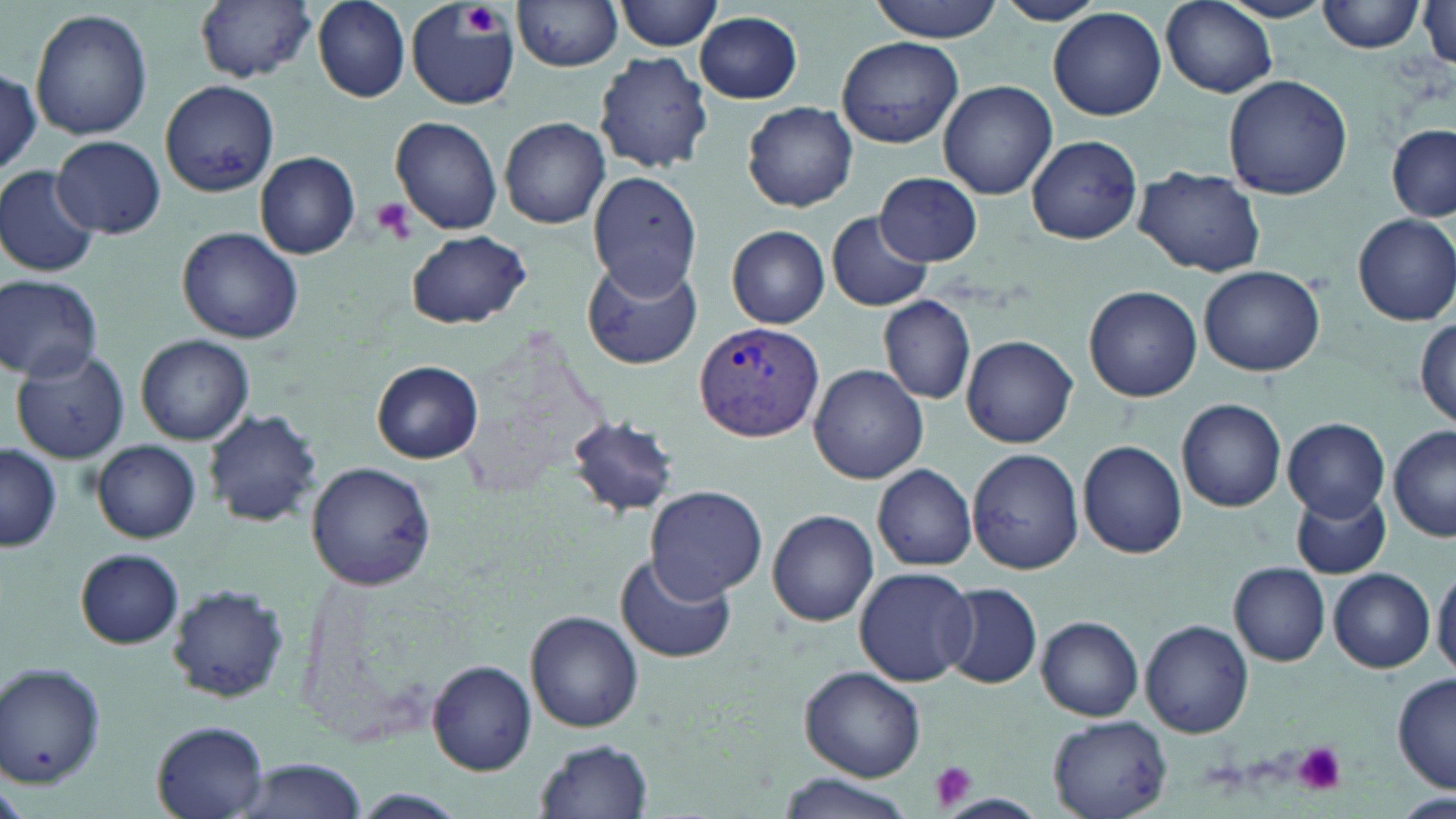
slide_level_diagnosis: Plasmodium vivax
platelet_locations: 'approximate bounding boxes as [x1, y1, x2, y2] in pixels: [460, 6, 506, 34], [370, 197, 416, 245], [1294, 742, 1347, 794], [929, 761, 978, 812]'
modality: light microscopy
preparation: thin blood smear
image_size: 1456×819 pixels
stain: May-Grünwald-Giemsa
plasmodium_vivax_infected_red_blood_cell_locations: 'approximate bounding boxes as [x1, y1, x2, y2] in pixels: [694, 321, 825, 443]'
magnification: 1000x
uninfected_red_blood_cell_locations: 'approximate bounding boxes as [x1, y1, x2, y2] in pixels: [311, 0, 411, 102], [615, 0, 724, 52], [870, 0, 1001, 41], [992, 0, 1105, 26], [1161, 0, 1278, 99], [1219, 0, 1335, 23], [1317, 0, 1424, 54], [195, 1, 316, 83], [515, 1, 624, 72], [407, 2, 519, 112], [1418, 4, 1456, 71], [30, 7, 152, 142], [1048, 8, 1167, 120], [695, 12, 803, 103], [837, 35, 963, 149], [594, 51, 714, 173], [0, 72, 42, 172], [1223, 74, 1353, 201], [160, 79, 279, 196], [938, 80, 1057, 200], [741, 102, 862, 212], [389, 116, 503, 236], [500, 116, 610, 228], [1386, 124, 1456, 222], [52, 135, 166, 238], [1026, 135, 1141, 244], [255, 150, 360, 258], [0, 166, 100, 276], [1133, 166, 1266, 277], [588, 171, 701, 298], [875, 172, 982, 265], [826, 210, 933, 312], [1353, 213, 1456, 326], [726, 224, 829, 327], [177, 226, 304, 344], [406, 229, 530, 329], [582, 255, 703, 371], [1198, 265, 1327, 377], [0, 275, 104, 383], [1082, 284, 1202, 401], [878, 294, 975, 404], [1414, 317, 1455, 428], [136, 333, 253, 443], [963, 335, 1078, 448], [11, 348, 132, 464], [372, 361, 483, 463], [809, 364, 928, 483], [1176, 398, 1287, 511], [203, 408, 323, 528], [566, 413, 679, 517], [1283, 417, 1390, 519], [1389, 426, 1456, 543], [91, 438, 202, 542], [1077, 439, 1187, 557], [1, 444, 61, 551], [967, 448, 1084, 575], [305, 462, 436, 590], [872, 464, 977, 571], [643, 485, 767, 603], [1292, 487, 1391, 580], [768, 509, 878, 626], [76, 549, 184, 649], [615, 553, 736, 664], [1229, 563, 1331, 666], [1432, 564, 1456, 676], [853, 567, 976, 686], [1328, 567, 1435, 672], [163, 582, 291, 705], [943, 584, 1042, 689], [526, 609, 643, 732], [1037, 616, 1144, 720], [1141, 619, 1254, 737], [0, 658, 108, 791], [426, 660, 537, 776], [800, 667, 928, 781], [1393, 672, 1455, 794], [1049, 715, 1173, 819], [151, 721, 270, 818], [535, 738, 653, 818], [230, 757, 372, 819], [777, 774, 917, 819], [345, 789, 467, 819], [939, 793, 1046, 816]'
field_of_view: single